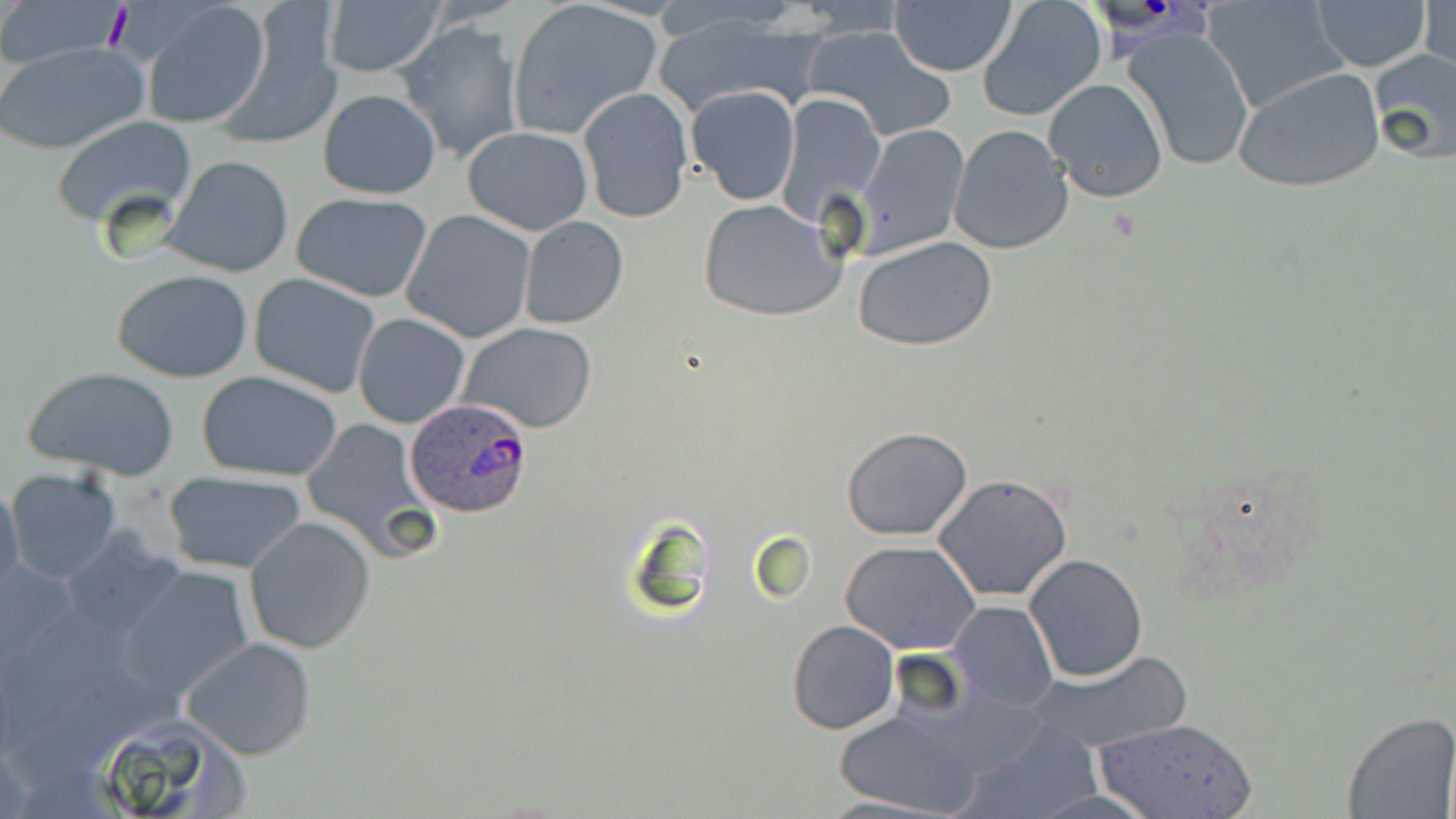

slide-level diagnosis = Plasmodium ovale
stain = May-Grünwald-Giemsa
image size = 1456×819 pixels
preparation = thin blood smear
magnification = 1000x
uninfected red blood cell locations = approximate bounding boxes as (x1, y1, x2, y2) in pixels: (0, 0, 129, 65), (141, 1, 272, 127), (320, 1, 444, 78), (508, 1, 663, 138), (1312, 1, 1431, 71), (889, 2, 1018, 77), (1203, 2, 1349, 112), (1421, 2, 1453, 80), (977, 3, 1105, 122), (219, 5, 344, 146), (655, 8, 816, 115), (395, 19, 525, 165), (802, 27, 956, 142), (1122, 28, 1256, 171), (0, 39, 150, 155), (1367, 48, 1456, 164), (18, 65, 164, 210), (1234, 67, 1385, 194), (1042, 78, 1169, 203), (685, 86, 801, 205), (578, 87, 693, 223), (317, 90, 439, 199), (776, 92, 887, 225), (734, 104, 870, 289), (53, 115, 196, 228), (856, 124, 969, 254), (948, 124, 1074, 256), (463, 127, 593, 235), (163, 156, 294, 277), (292, 192, 433, 303), (697, 198, 846, 321), (402, 210, 537, 343), (519, 216, 628, 328), (854, 237, 997, 352), (112, 270, 255, 383), (249, 273, 381, 397), (352, 311, 470, 428), (459, 322, 596, 433), (23, 365, 182, 481), (198, 371, 343, 482), (302, 415, 436, 558), (842, 427, 972, 540), (6, 468, 122, 586), (165, 470, 307, 573), (933, 474, 1073, 602), (0, 482, 24, 599), (245, 516, 376, 653), (60, 527, 187, 645), (841, 539, 981, 655), (1023, 554, 1147, 682), (118, 565, 257, 701), (946, 602, 1059, 713), (788, 620, 899, 735), (181, 635, 317, 759), (1023, 651, 1192, 752), (82, 705, 250, 815), (833, 708, 984, 817), (1340, 712, 1453, 819), (1092, 716, 1261, 819), (959, 721, 1108, 819), (813, 796, 955, 818)
field of view = one of a larger specimen
Plasmodium ovale-infected red blood cell locations = approximate bounding boxes as (x1, y1, x2, y2) in pixels: (405, 399, 535, 519)
modality = light microscopy